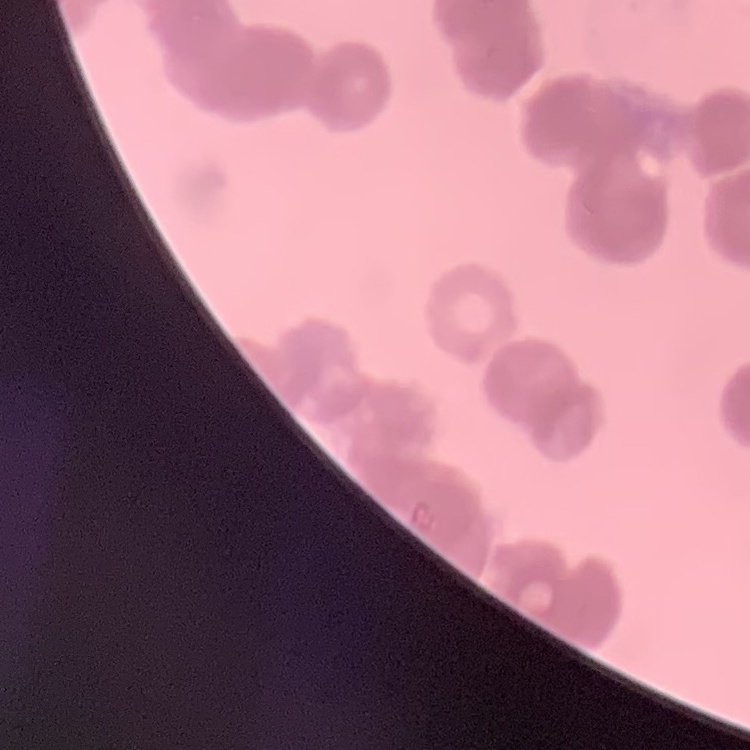
The erythrocytes show rouleaux formation. Square crop of a larger photomicrograph. Thin blood film. Field's or Giemsa stain.